Describe the morphology of the red blood cells.
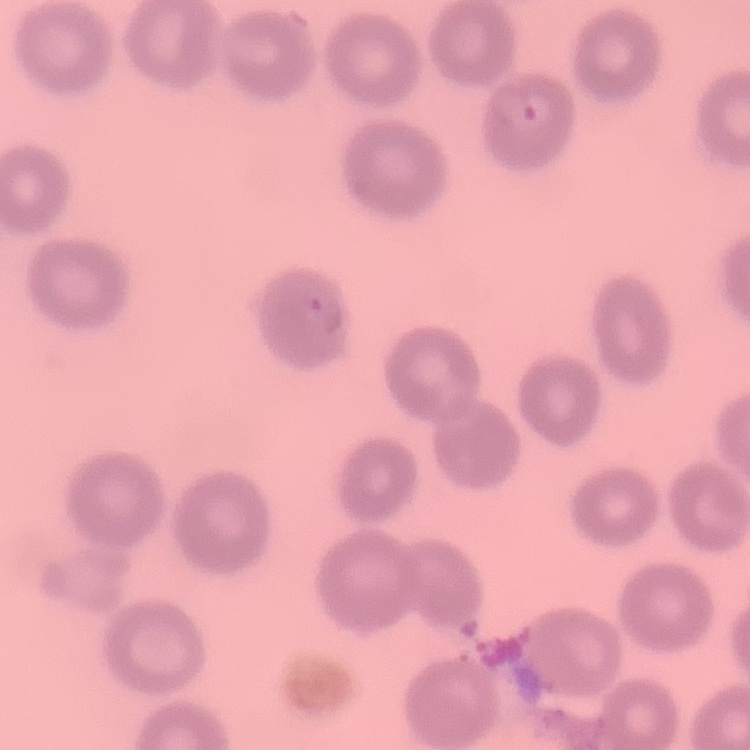
They show no rouleaux formation.

{
  "image_type": "square crop of a larger photomicrograph",
  "preparation": "thin blood smear",
  "stain": "Field's or Giemsa"
}